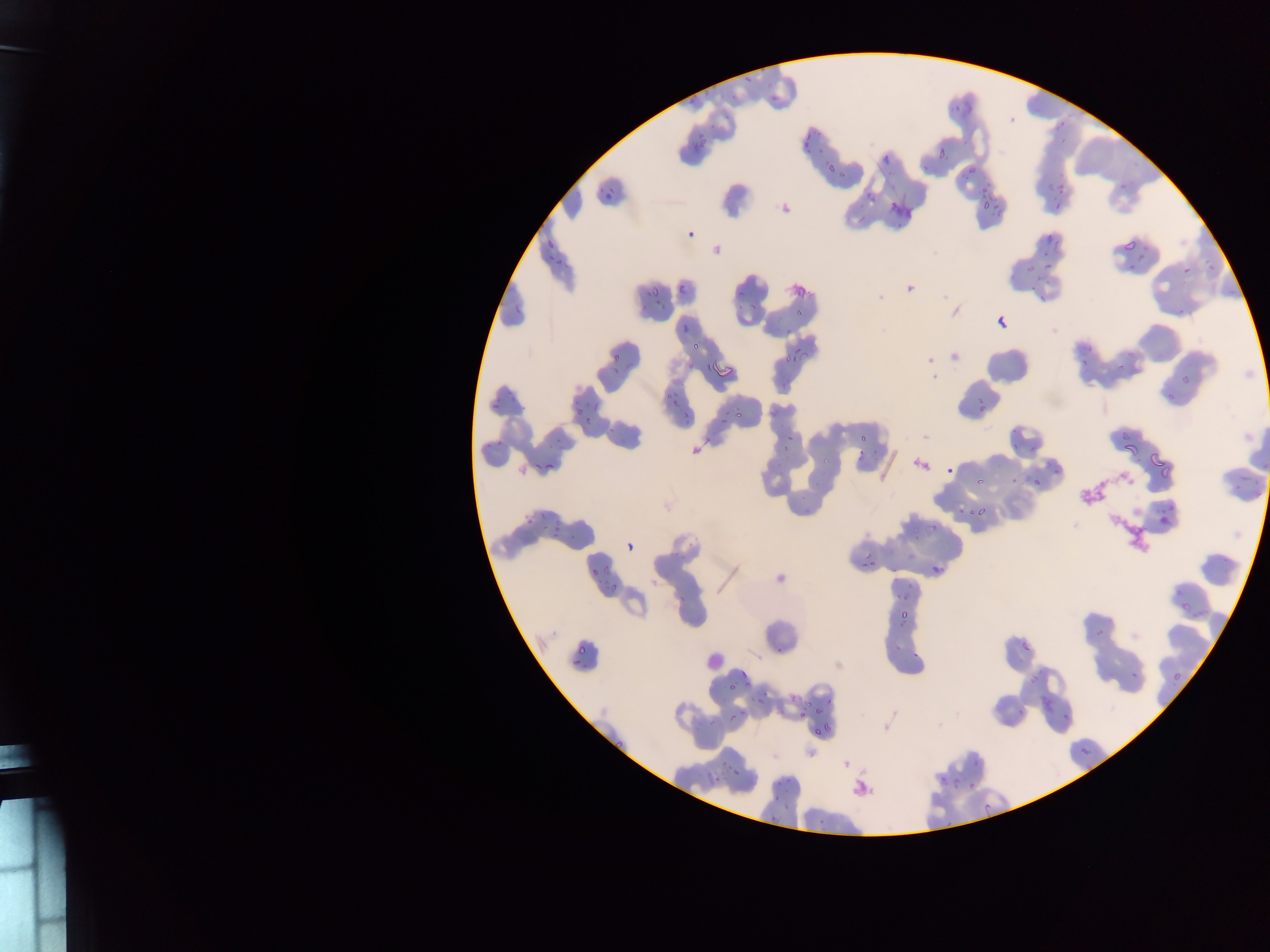

Approximate bounding boxes as [left, top, right, bottom] in pixels.
Summary:
  - Plasmodium parasite locations: [1058, 120, 1065, 128], [685, 124, 723, 156], [936, 133, 952, 166], [802, 135, 813, 146], [960, 161, 982, 191], [1039, 175, 1061, 193], [595, 185, 612, 207], [973, 194, 1007, 213], [1054, 204, 1061, 212], [682, 228, 696, 238], [1048, 233, 1056, 240], [546, 239, 554, 249], [1123, 240, 1135, 251], [1126, 249, 1155, 279], [1016, 254, 1053, 276], [1182, 267, 1191, 276], [680, 283, 688, 293], [1027, 284, 1054, 309], [649, 287, 659, 296], [648, 290, 680, 317], [794, 305, 811, 319], [1163, 306, 1196, 317], [998, 317, 1007, 327], [670, 328, 692, 350], [685, 335, 707, 368], [779, 339, 809, 370], [1075, 344, 1100, 371], [1110, 344, 1152, 373], [607, 353, 631, 372], [660, 370, 684, 403], [1180, 370, 1200, 394], [1165, 377, 1189, 403], [575, 396, 594, 415], [493, 400, 500, 409], [728, 405, 756, 421], [580, 417, 598, 432], [850, 423, 884, 467], [781, 432, 802, 453], [1113, 435, 1137, 461], [1008, 438, 1021, 451], [1140, 449, 1167, 478], [1043, 453, 1067, 477], [546, 461, 554, 471], [945, 465, 954, 474], [1231, 465, 1260, 492], [975, 476, 984, 485], [1027, 477, 1039, 491], [1161, 504, 1192, 529], [969, 505, 980, 516], [524, 515, 540, 531], [545, 522, 573, 543], [626, 541, 640, 552], [858, 544, 879, 573], [927, 564, 937, 583], [590, 567, 600, 577], [606, 591, 621, 601], [894, 597, 913, 630], [1181, 603, 1191, 613], [573, 640, 593, 664], [776, 644, 786, 653], [1170, 651, 1200, 691], [572, 658, 582, 666], [1122, 668, 1149, 685], [739, 670, 749, 680], [750, 686, 778, 713], [796, 692, 839, 722], [1041, 697, 1053, 710], [728, 712, 738, 721], [815, 726, 826, 736], [1080, 746, 1090, 756], [707, 757, 737, 783], [945, 765, 969, 792], [772, 778, 781, 787], [968, 782, 976, 791], [768, 813, 778, 823], [817, 818, 826, 827] | approximate [x, y] pixel centers of objects too small to bound: [1122, 186]
  - Leukocyte locations: [704, 649, 726, 670]
  - Field of view: single
  - Image size: 1270×952 pixels
  - Preparation: thin blood film
  - Country: Ghana
  - Capture: mobile-phone photograph through a microscope